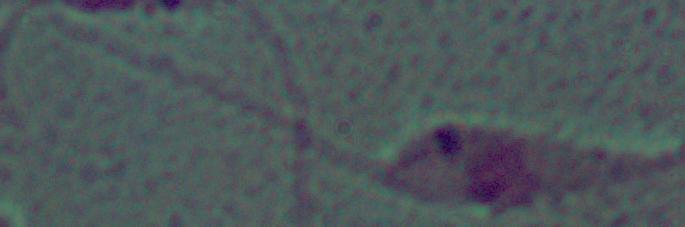
A Leishmania parasite is seen. Captured at 1000x magnification. Micrograph.